Identify the cell.
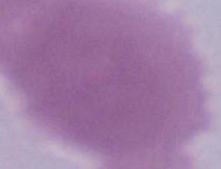
An erythrocyte.

modality = micrograph
magnification = 1000x